Classify this cell by malaria status.
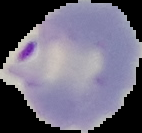

It is parasitized.

Image is 142×133 pixels. Cell region segmented out of the field of view; the surrounding area is masked to black. From a thin blood film.